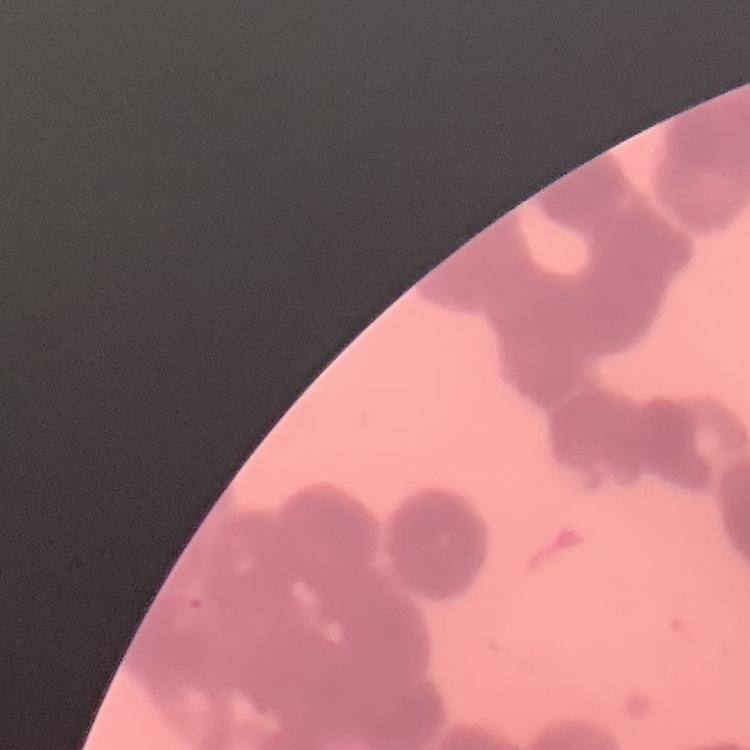
The erythrocytes exhibit rouleaux formation. Thin blood smear. Stained with either Field's or Giemsa. Square crop of a larger photomicrograph.